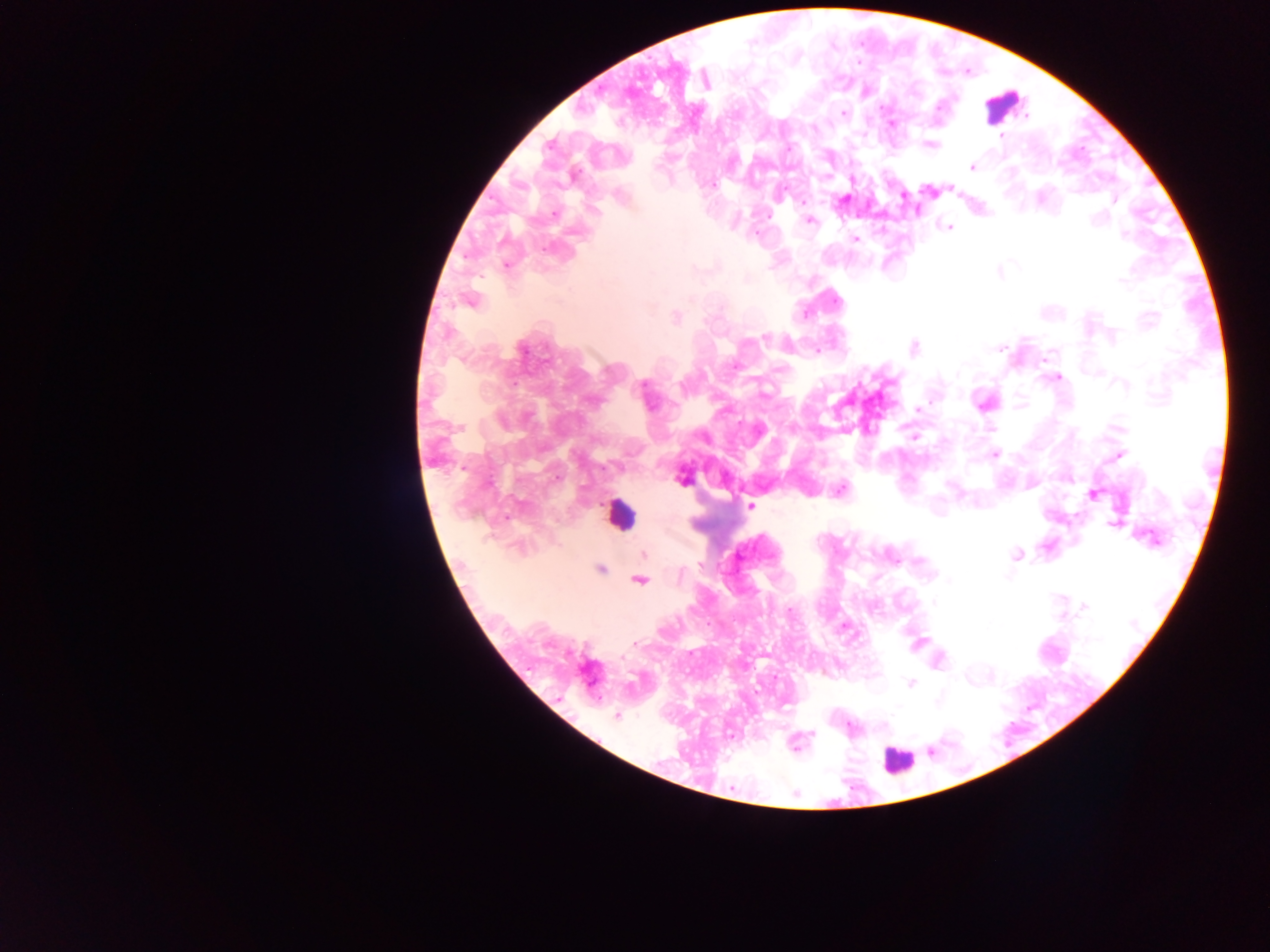
preparation: thick blood film
leukocyte_locations: 'approximate centers as x y in pixels: 1004 105; 620 515; 897 760'
capture: mobile-phone photograph through a microscope
field_of_view: single
country: Ghana
image_size: 1270×952 pixels
plasmodium_parasite_locations: 'approximate centers as x y in pixels: 865 93; 881 108; 843 113; 892 125; 813 128; 1002 136; 931 145; 788 150; 972 167; 713 184; 950 188; 928 192; 903 197; 845 199; 1114 200; 803 202; 595 210; 554 213; 767 215; 809 221; 949 228; 1123 235; 855 239; 506 264; 999 272; 1121 280; 469 301; 804 313; 676 317; 764 339; 523 348; 913 348; 999 349; 818 351; 1059 378; 917 409; 990 428; 915 437; 995 454; 1119 455; 683 479; 488 484; 842 489; 1093 495; 751 506; 507 516; 1113 524; 644 554; 1015 554; 700 565; 600 569; 639 580; 1085 607; 790 609; 844 626; 634 643; 910 683; 616 716; 850 728; 814 734; 796 743'